Assess this cell for malaria.
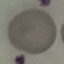

It is uninfected.

{
  "stain": "Giemsa",
  "image_type": "automatically extracted cell patch, resized to 64 × 64 pixels",
  "preparation": "thin blood film",
  "capture": "smartphone camera at the microscope eyepiece"
}